Classify this cell by malaria status.
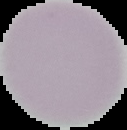
Uninfected.

Summary:
  - Image type: cell region segmented out of the field of view; surrounding area masked to black
  - Image size: 127×130 pixels
  - Preparation: thin blood smear